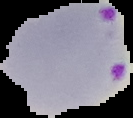

Image is 133×118 pixels. From a thin blood film. Segmented cell region on a black background. Result: Plasmodium parasites identified.